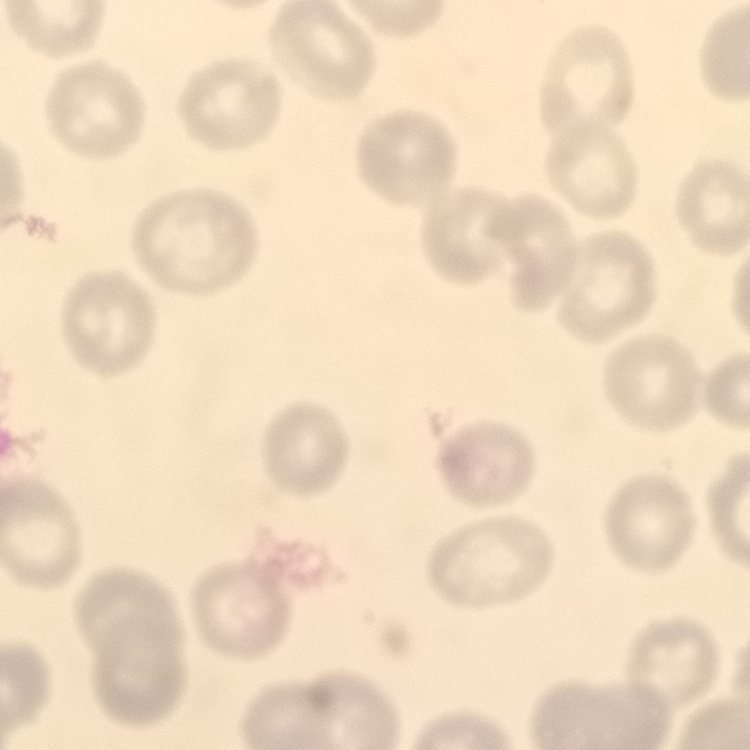

Summary:
  - Erythrocyte morphology: no rouleaux formation
  - Stain: Field's or Giemsa
  - Preparation: thin blood film
  - Image type: square crop of a larger photomicrograph